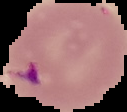

image size = 127×112 pixels
image type = segmented cell region with the area outside set to black
malaria status = parasitized
preparation = thin blood smear